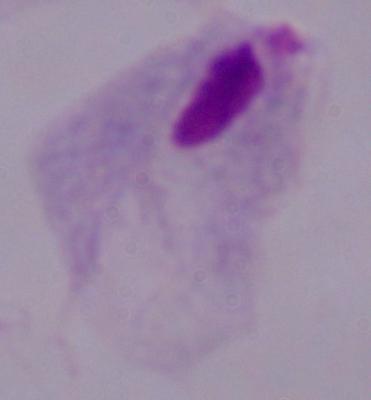
Summary:
  - Magnification: 1000x
  - Identification: trichomonad
  - Modality: photomicrograph